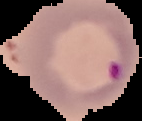

Malaria status: parasitized. Image is 142×121 pixels. Cell region segmented out of the field of view; the surrounding area is masked to black. From a thin blood smear.